Evaluate for Plasmodium parasites.
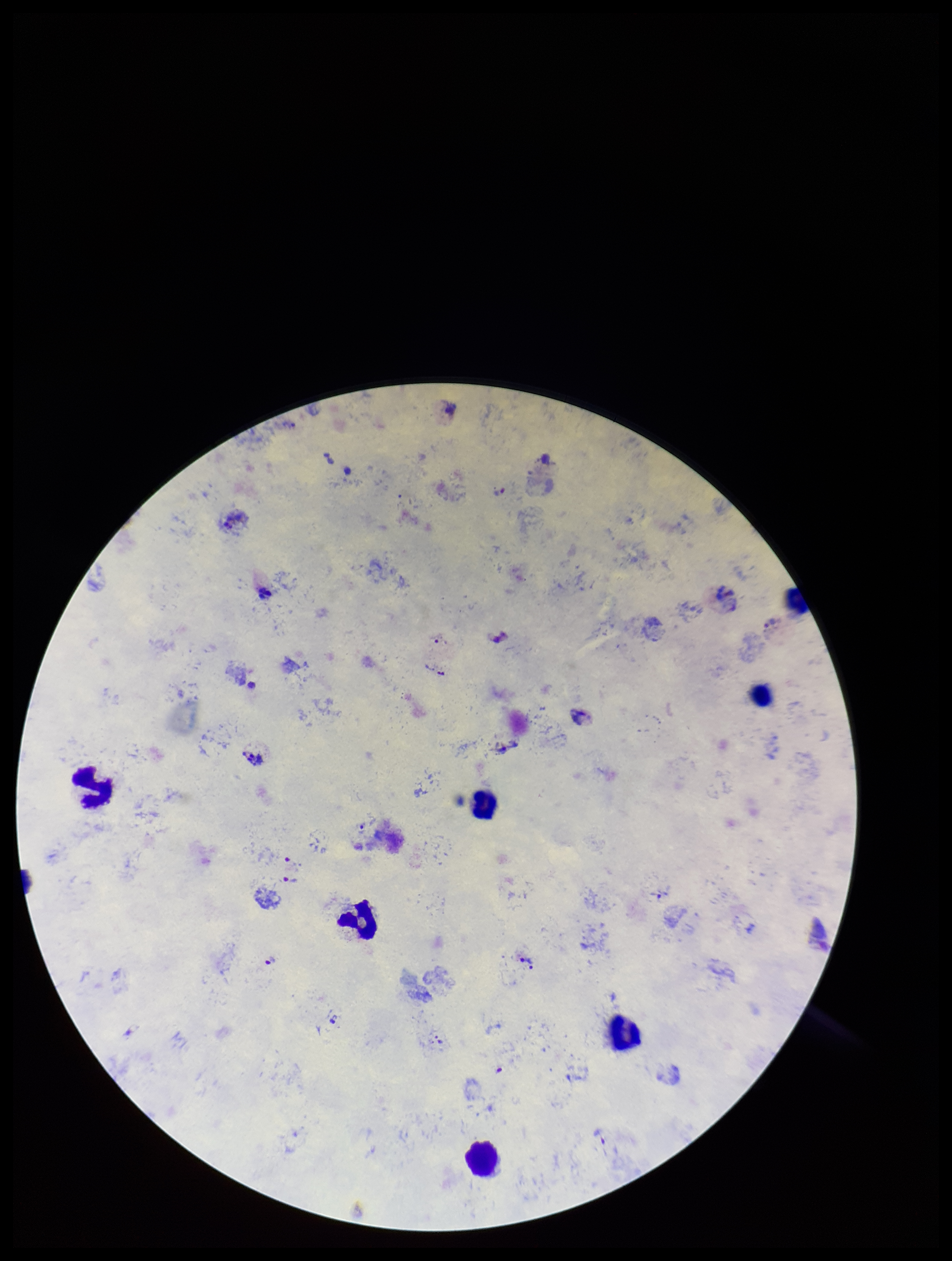
Detected.

Stained with Giemsa. Preparation: thick. Smartphone photograph taken through the eyepiece of a microscope. Parasite count: 11. Image is 952×1261 pixels. One field from this slide. Patient malaria status: positive. Species reported for this patient: Plasmodium vivax. Leukocyte count: 7.